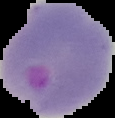 From a thin blood smear. Cell region segmented out of the field of view; the surrounding area is masked to black. Result: Plasmodium parasites detected. Image is 115×118 pixels.